Assess this cell for malaria.
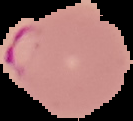

Parasitized.

Summary:
  - Image type: segmented cell region on a black background
  - Preparation: thin blood film
  - Image size: 133×121 pixels